Comment on the morphology of the erythrocytes.
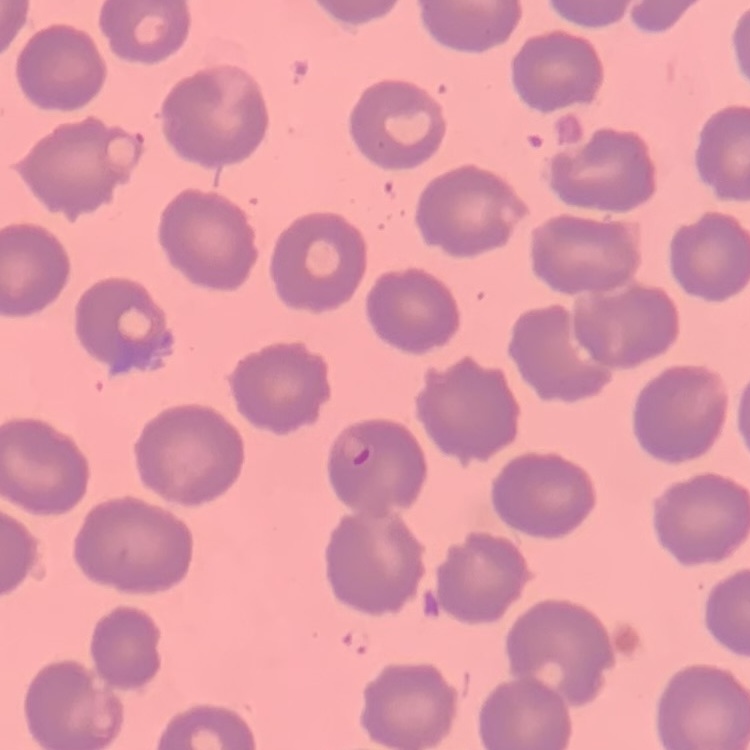

They show no rouleaux formation.

Field's or Giemsa stain. Thin blood smear. Square crop of a larger photomicrograph.